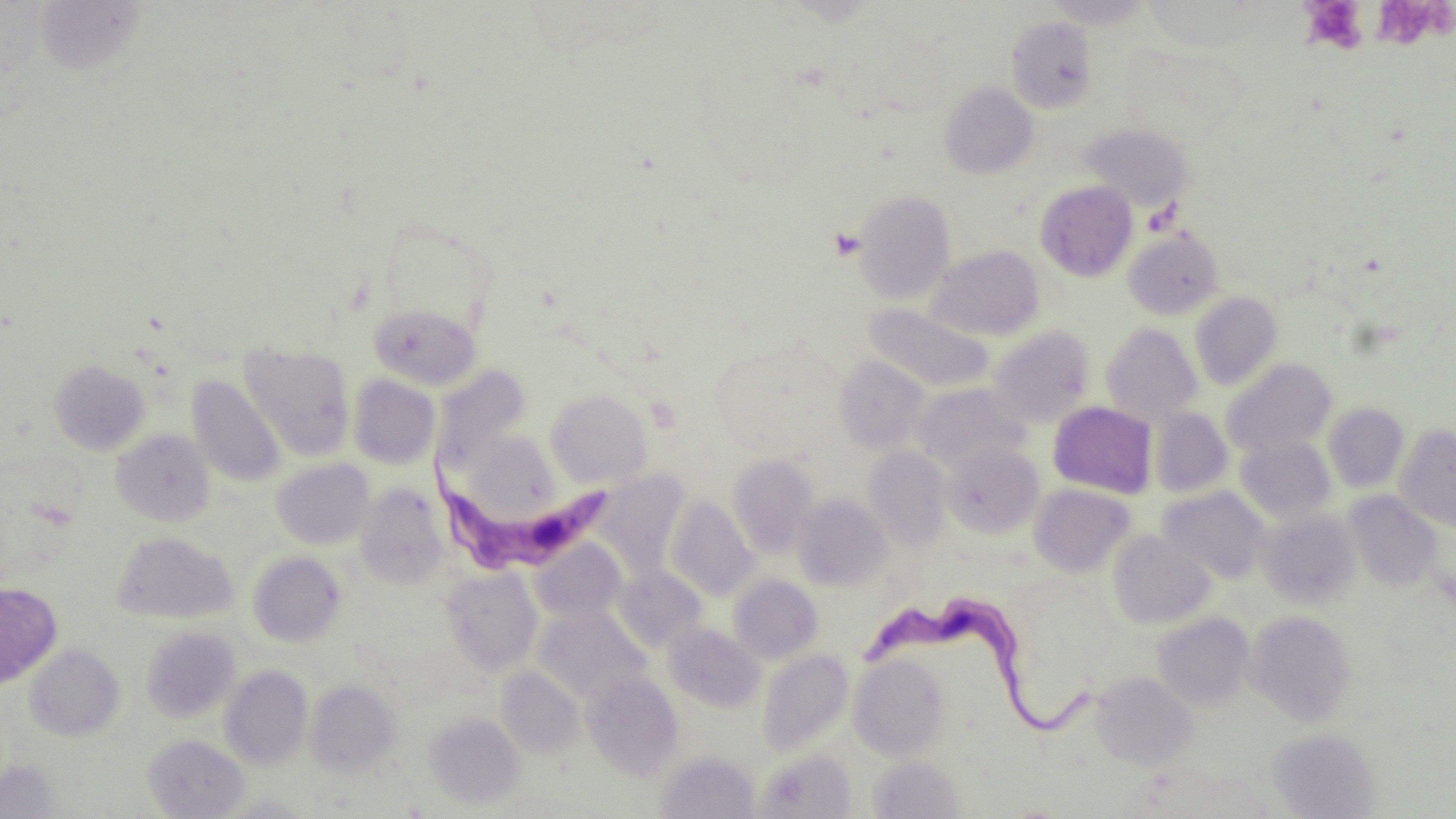

Summary:
  - Coordinate format: approximate bounding boxes as named x1/y1/x2/y2 corners in pixels
  - Platelet locations: (x1=1306, y1=0, x2=1367, y2=56), (x1=1377, y1=0, x2=1453, y2=52), (x1=830, y1=227, x2=865, y2=260)
  - Uninfected red blood cell locations: (x1=1042, y1=0, x2=1154, y2=28), (x1=35, y1=2, x2=147, y2=77), (x1=1005, y1=17, x2=1099, y2=113), (x1=829, y1=19, x2=955, y2=120), (x1=939, y1=83, x2=1038, y2=179), (x1=1082, y1=123, x2=1193, y2=213), (x1=1035, y1=180, x2=1138, y2=281), (x1=853, y1=189, x2=956, y2=304), (x1=377, y1=219, x2=500, y2=336), (x1=1123, y1=228, x2=1225, y2=320), (x1=927, y1=245, x2=1044, y2=341), (x1=1190, y1=292, x2=1283, y2=390), (x1=864, y1=303, x2=995, y2=394), (x1=368, y1=304, x2=482, y2=389), (x1=1100, y1=323, x2=1203, y2=424), (x1=988, y1=325, x2=1096, y2=426), (x1=240, y1=345, x2=355, y2=460), (x1=834, y1=356, x2=931, y2=453), (x1=1223, y1=358, x2=1337, y2=459), (x1=49, y1=359, x2=150, y2=455), (x1=431, y1=365, x2=531, y2=473), (x1=348, y1=374, x2=440, y2=469), (x1=188, y1=375, x2=286, y2=487), (x1=912, y1=383, x2=1031, y2=474), (x1=545, y1=389, x2=654, y2=489), (x1=1048, y1=401, x2=1158, y2=499), (x1=1322, y1=403, x2=1409, y2=493), (x1=1150, y1=407, x2=1232, y2=498), (x1=1395, y1=424, x2=1456, y2=533), (x1=111, y1=429, x2=215, y2=526), (x1=468, y1=434, x2=560, y2=525), (x1=1236, y1=436, x2=1337, y2=524), (x1=941, y1=442, x2=1044, y2=539), (x1=864, y1=447, x2=951, y2=550), (x1=727, y1=453, x2=820, y2=557), (x1=271, y1=459, x2=374, y2=550), (x1=591, y1=471, x2=690, y2=576), (x1=1029, y1=483, x2=1136, y2=577), (x1=356, y1=484, x2=450, y2=589), (x1=1158, y1=486, x2=1271, y2=585), (x1=1343, y1=491, x2=1445, y2=593), (x1=792, y1=492, x2=893, y2=590), (x1=666, y1=497, x2=759, y2=600), (x1=1259, y1=510, x2=1361, y2=610), (x1=1108, y1=530, x2=1215, y2=630), (x1=113, y1=531, x2=237, y2=624), (x1=530, y1=539, x2=626, y2=625), (x1=248, y1=552, x2=346, y2=647), (x1=442, y1=567, x2=542, y2=675), (x1=613, y1=567, x2=707, y2=652), (x1=729, y1=574, x2=823, y2=663), (x1=0, y1=582, x2=62, y2=689), (x1=533, y1=607, x2=649, y2=703), (x1=1246, y1=609, x2=1357, y2=727), (x1=1152, y1=612, x2=1255, y2=710), (x1=663, y1=622, x2=764, y2=712), (x1=141, y1=626, x2=241, y2=723), (x1=25, y1=644, x2=125, y2=741), (x1=757, y1=648, x2=854, y2=758), (x1=849, y1=654, x2=951, y2=761), (x1=220, y1=665, x2=313, y2=770), (x1=497, y1=666, x2=584, y2=758), (x1=583, y1=671, x2=684, y2=780), (x1=1091, y1=672, x2=1199, y2=770), (x1=306, y1=680, x2=402, y2=777), (x1=425, y1=712, x2=525, y2=808), (x1=1268, y1=728, x2=1381, y2=818), (x1=143, y1=734, x2=249, y2=818), (x1=756, y1=749, x2=856, y2=819), (x1=655, y1=750, x2=760, y2=819), (x1=868, y1=756, x2=963, y2=818), (x1=0, y1=758, x2=65, y2=817)
  - Trypanosoma brucei locations: (x1=424, y1=439, x2=617, y2=572), (x1=865, y1=596, x2=1105, y2=743)
  - Slide-level diagnosis: Trypanosoma brucei
  - Magnification: 1000x
  - Preparation: thin blood film
  - Image size: 1456×819 pixels
  - Field of view: single
  - Modality: light microscopy
  - Stain: May-Grünwald-Giemsa